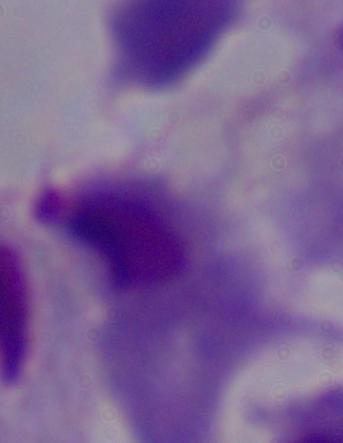
Captured at 1000x magnification. A trichomonad is shown. Photomicrograph.